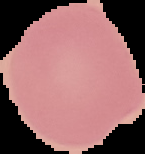 Image is 145×154 pixels. Result: no Plasmodium parasites detected. The area outside the segmented cell region is set to black. From a thin blood film.